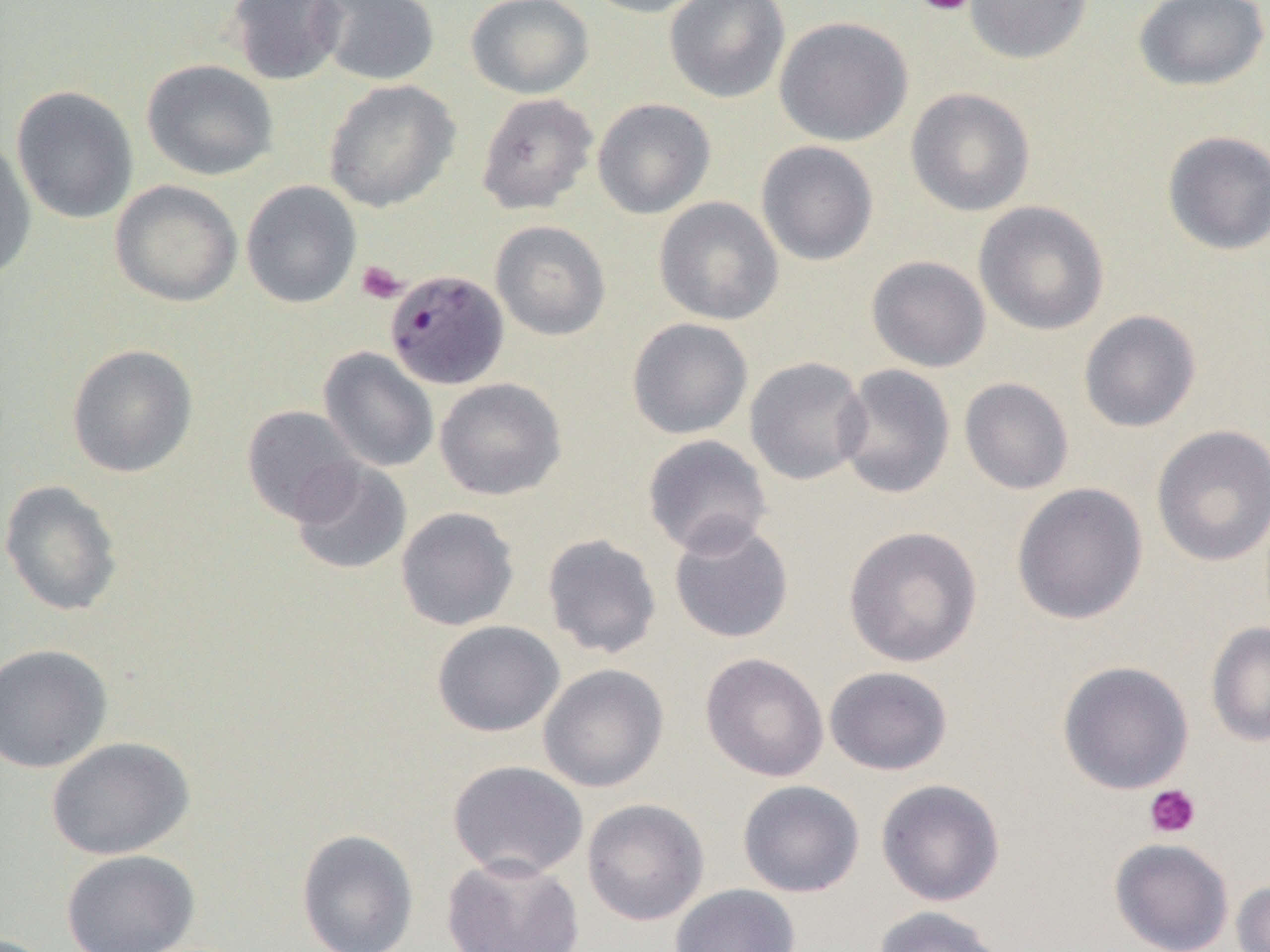

Approximate bounding boxes as (x1,y1)-(x2,y2) corner pairs in pixels. Platelet locations: (913,0)-(976,17), (356,260)-(407,304), (1144,784)-(1201,838). Plasmodium malariae-infected red blood cell locations: (384,268)-(509,390). Uninfected red blood cell locations: (227,0)-(346,86), (315,0)-(440,86), (464,0)-(594,99), (580,0)-(711,18), (664,0)-(791,103), (964,0)-(1093,64), (1133,0)-(1269,91), (774,16)-(913,146), (142,59)-(279,181), (323,79)-(460,212), (11,85)-(139,224), (905,87)-(1035,217), (475,92)-(598,215), (592,98)-(715,219), (1162,130)-(1270,255), (0,139)-(37,282), (755,141)-(879,266), (109,179)-(242,307), (240,180)-(361,308), (654,197)-(784,325), (974,200)-(1110,336), (490,220)-(611,341), (866,255)-(991,372), (1078,309)-(1202,433), (627,317)-(753,440), (66,343)-(198,478), (318,347)-(439,473), (744,356)-(871,486), (835,363)-(956,500), (434,377)-(567,500), (959,378)-(1074,495), (241,404)-(364,524), (1151,424)-(1270,567), (642,434)-(773,558), (289,459)-(412,576), (0,479)-(123,616), (1011,482)-(1148,625), (395,506)-(519,631), (668,519)-(794,645), (842,525)-(983,668), (541,533)-(662,659), (431,620)-(565,737), (1206,621)-(1270,747), (0,643)-(113,774), (700,652)-(829,782), (1057,660)-(1194,795), (538,663)-(669,793), (824,666)-(953,776), (46,736)-(195,860), (447,759)-(589,880), (875,778)-(1006,906), (737,779)-(865,898), (582,798)-(710,926), (296,828)-(419,952), (1109,837)-(1234,952), (61,849)-(200,952), (442,852)-(585,951), (1231,880)-(1270,952), (670,883)-(801,952), (871,905)-(1007,952). Slide-level diagnosis: Plasmodium malariae. Image is 1270×952 pixels. 1000x magnification. Single field of view. Thin blood film. Optical microscopy.